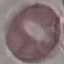
{
  "malaria_status": "uninfected",
  "stain": "Giemsa",
  "image_type": "automatically extracted cell patch, resized to 64 × 64 pixels",
  "capture": "smartphone through the microscope eyepiece",
  "preparation": "thin blood smear"
}